Evaluate for Plasmodium parasites.
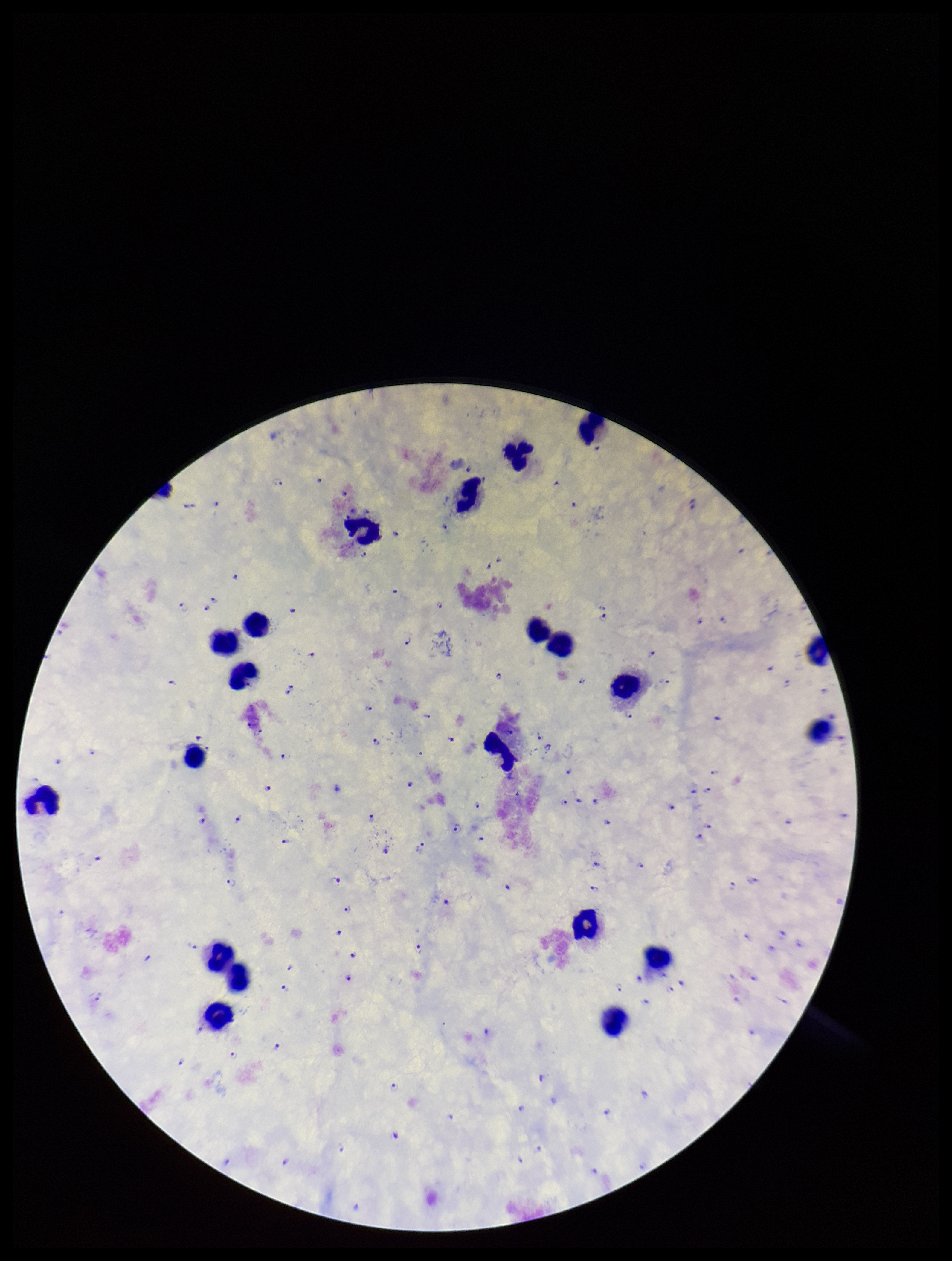

Detected.

Summary:
  - Field of view: one from this slide
  - Patient malaria status: positive
  - Preparation: thick blood smear
  - Stain: Giemsa
  - Species reported for this patient: Plasmodium falciparum
  - Leukocyte count: 19
  - Image size: 952×1261 pixels
  - Parasite count: 112
  - Capture: smartphone photograph through the microscope eyepiece